Name the parasite shown.
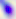
This is Toxoplasma gondii.

400x magnification. Photomicrograph.